Outline each Plasmodium falciparum-infected red blood cell.
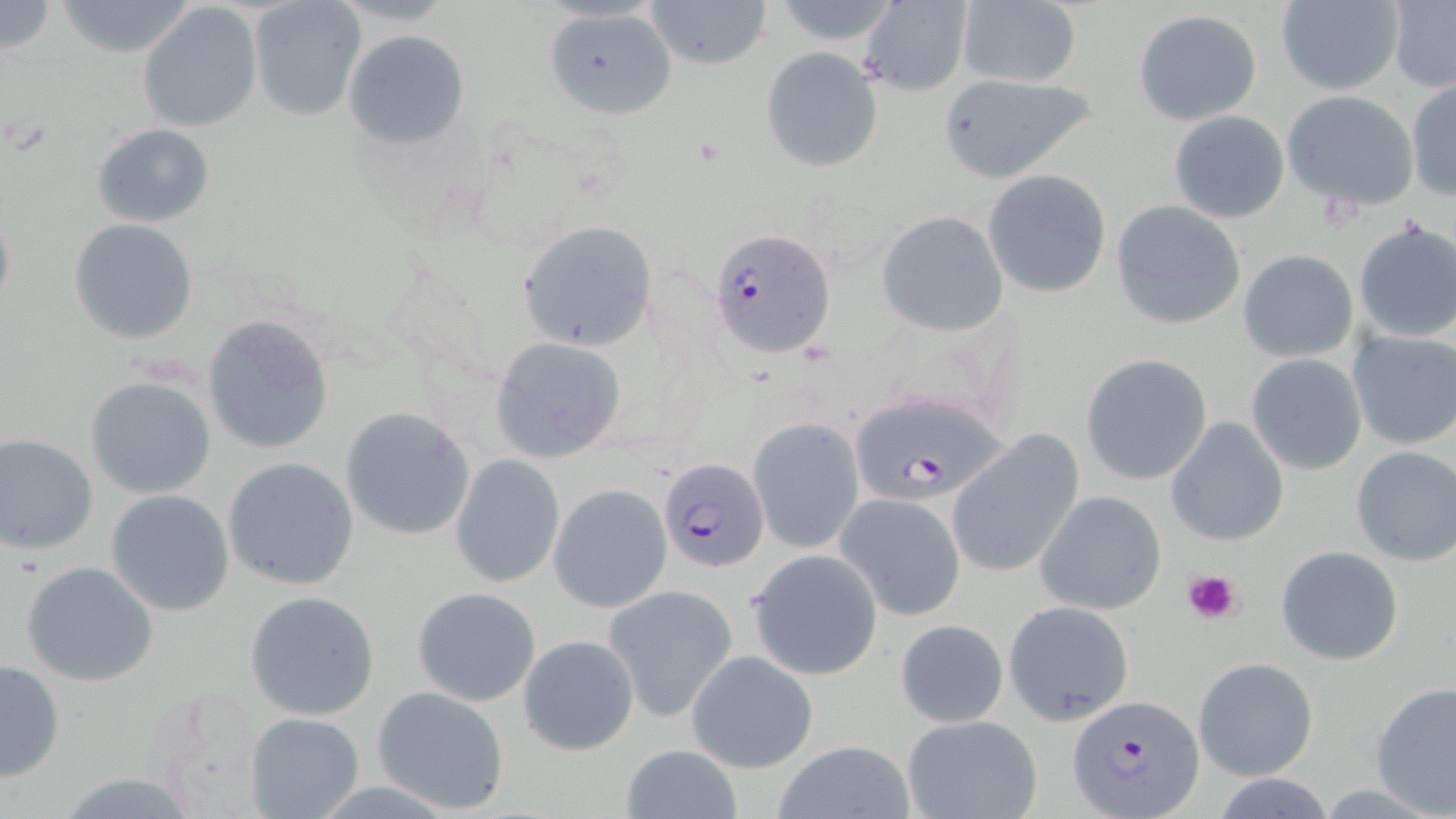

Approximate bounding boxes as [x1, y1, x2, y2] in pixels.
Plasmodium falciparum-infected red blood cells: [710, 226, 835, 357], [849, 391, 1013, 506], [659, 457, 770, 573], [1069, 693, 1207, 818].

slide-level diagnosis = Plasmodium falciparum
modality = optical microscopy
image size = 1456×819 pixels
stain = May-Grünwald-Giemsa
field of view = single
uninfected red blood cell locations = approximate bounding boxes as [x1, y1, x2, y2] in pixels: [0, 0, 59, 55], [53, 0, 200, 58], [643, 0, 773, 69], [859, 0, 973, 97], [1273, 1, 1404, 95], [248, 2, 364, 121], [954, 2, 1085, 88], [1387, 2, 1456, 91], [138, 4, 263, 133], [538, 6, 681, 118], [1133, 8, 1262, 125], [343, 29, 471, 151], [760, 46, 884, 173], [935, 72, 1099, 182], [1405, 79, 1455, 201], [1281, 90, 1419, 210], [1168, 110, 1290, 223], [92, 124, 217, 227], [982, 169, 1112, 299], [0, 200, 15, 323], [1111, 200, 1246, 329], [876, 211, 1009, 336], [69, 219, 199, 344], [517, 220, 658, 351], [1351, 220, 1456, 345], [1237, 249, 1359, 363], [202, 315, 334, 454], [1346, 330, 1456, 451], [488, 335, 627, 462], [1081, 352, 1214, 486], [1245, 354, 1367, 475], [84, 375, 217, 499], [340, 406, 476, 540], [1165, 417, 1289, 547], [749, 418, 863, 553], [946, 430, 1084, 580], [0, 434, 98, 555], [1349, 446, 1456, 566], [450, 456, 565, 586], [223, 457, 360, 591], [548, 485, 671, 613], [105, 490, 234, 616], [1034, 490, 1168, 615], [836, 493, 967, 621], [1276, 546, 1404, 664], [747, 549, 883, 680], [21, 561, 159, 687], [604, 584, 738, 720], [411, 586, 542, 707], [245, 590, 382, 721], [1003, 600, 1134, 723], [897, 618, 1010, 728], [518, 634, 638, 755], [687, 650, 817, 772], [1193, 657, 1318, 782], [1, 659, 66, 783], [1370, 682, 1456, 814], [143, 683, 271, 815], [371, 686, 511, 816], [245, 712, 364, 819], [901, 715, 1044, 819], [773, 740, 916, 818], [617, 744, 742, 817]
preparation = thin blood film
magnification = 1000x
platelet locations = approximate bounding boxes as [x1, y1, x2, y2] in pixels: [1180, 567, 1244, 626]